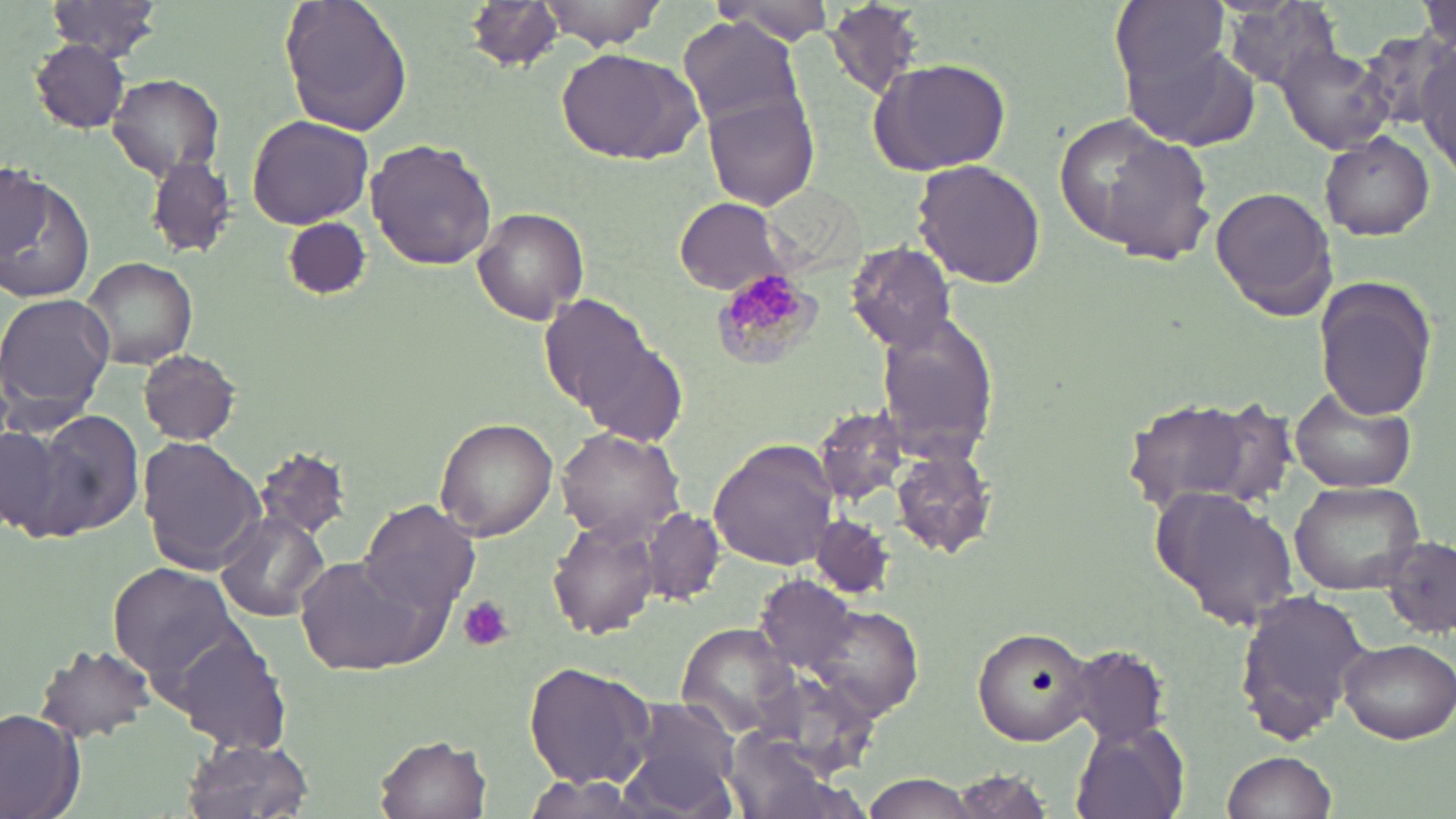

Summary:
  - Coordinate format: approximate bounding boxes as [x1, y1, x2, y2] in pixels
  - Uninfected red blood cell locations: [47, 0, 166, 61], [280, 0, 413, 138], [464, 0, 566, 72], [535, 0, 665, 51], [712, 0, 836, 47], [1114, 0, 1231, 94], [1421, 0, 1454, 71], [1220, 1, 1346, 88], [826, 2, 922, 99], [679, 18, 806, 136], [1412, 38, 1455, 170], [29, 39, 130, 132], [1124, 40, 1257, 149], [1276, 42, 1396, 153], [557, 47, 699, 163], [867, 57, 1013, 175], [107, 73, 225, 179], [702, 92, 821, 211], [246, 115, 373, 228], [1070, 120, 1216, 266], [1320, 134, 1435, 239], [366, 139, 496, 269], [146, 157, 238, 256], [912, 160, 1046, 289], [1, 164, 46, 259], [0, 172, 96, 303], [1212, 184, 1338, 321], [674, 198, 788, 292], [474, 208, 591, 325], [284, 218, 370, 300], [844, 242, 957, 354], [82, 256, 199, 369], [32, 265, 155, 391], [1313, 277, 1438, 419], [0, 291, 117, 428], [538, 293, 658, 416], [874, 312, 1001, 464], [572, 329, 689, 448], [137, 349, 240, 445], [1293, 390, 1417, 492], [1120, 397, 1275, 512], [813, 405, 908, 503], [32, 409, 146, 539], [435, 417, 559, 541], [3, 426, 58, 535], [556, 428, 687, 543], [137, 438, 265, 576], [708, 439, 839, 572], [255, 447, 350, 540], [892, 451, 994, 558], [1290, 479, 1425, 594], [1149, 486, 1300, 631], [357, 500, 480, 617], [643, 510, 724, 604], [213, 511, 329, 622], [810, 512, 893, 598], [549, 516, 665, 642], [1382, 538, 1456, 638], [294, 556, 440, 676], [109, 562, 240, 680], [757, 574, 858, 670], [1234, 587, 1374, 746], [137, 590, 279, 737], [803, 605, 924, 721], [681, 623, 798, 733], [972, 625, 1097, 746], [177, 636, 291, 754], [1336, 638, 1454, 745], [1060, 644, 1174, 746], [34, 645, 156, 743], [525, 662, 658, 790], [747, 672, 879, 782], [618, 698, 741, 815], [0, 708, 87, 819], [1071, 719, 1190, 819], [376, 733, 494, 819], [182, 735, 314, 819], [1223, 749, 1340, 819], [944, 770, 1059, 818], [864, 777, 977, 818], [516, 779, 647, 817]
  - Plasmodium malariae-infected red blood cell locations: [715, 269, 816, 367]
  - Platelet locations: [459, 595, 513, 651]
  - Slide-level diagnosis: Plasmodium malariae
  - Field of view: single
  - Image size: 1456×819 pixels
  - Preparation: thin blood smear
  - Modality: light microscopy
  - Stain: May-Grünwald-Giemsa
  - Magnification: 1000x